Give the position of every leukocyte visible.
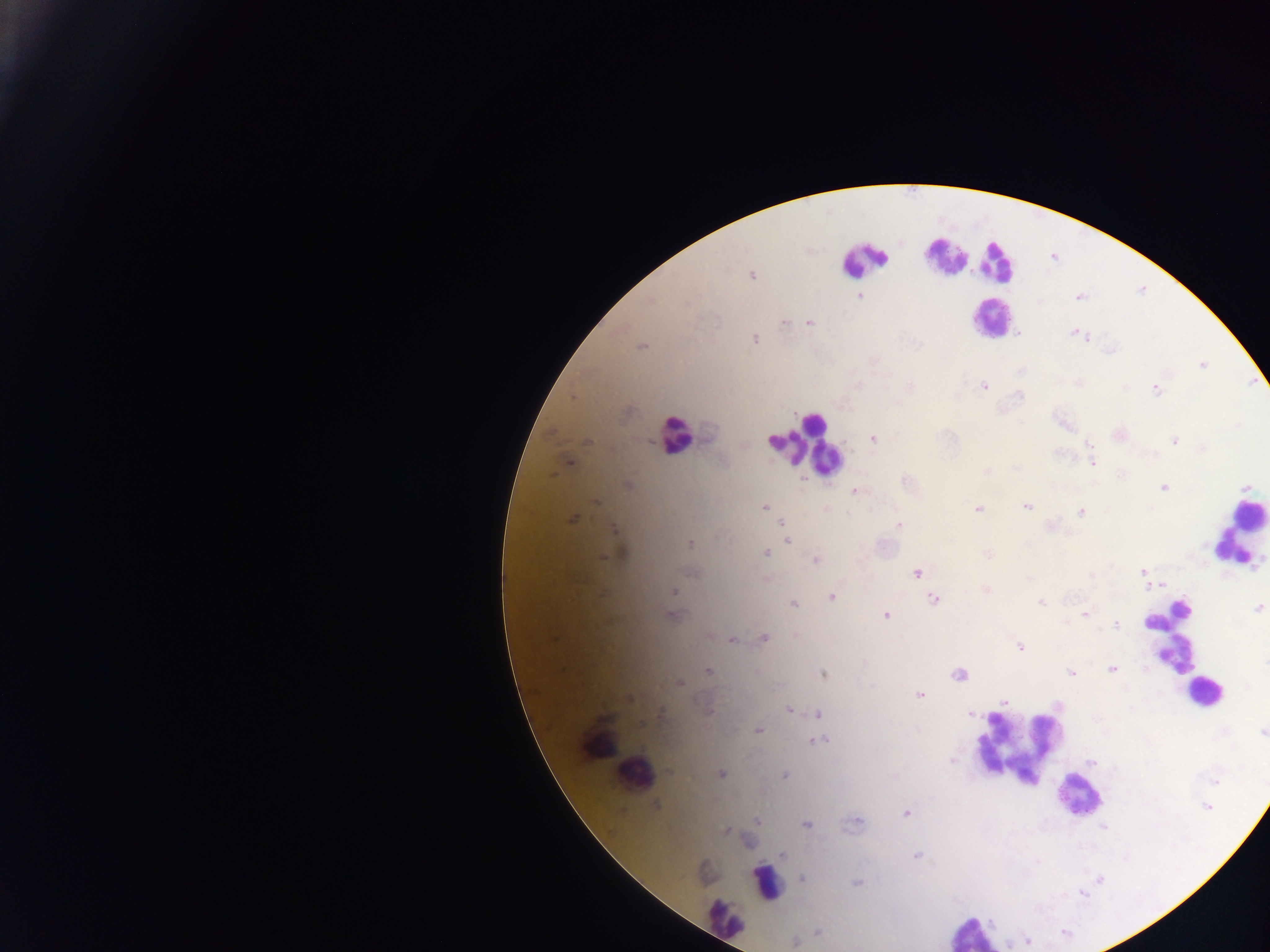
Approximate centers as {x, y} in pixels.
Leukocytes: {942, 255}, {862, 260}, {994, 262}, {989, 318}, {675, 435}, {803, 444}, {1239, 531}, {1172, 638}, {1202, 692}, {1016, 749}, {633, 772}, {1077, 797}, {765, 882}, {724, 919}, {971, 932}.

Malaria parasite locations: {752, 276}, {859, 295}, {1078, 298}, {784, 322}, {809, 323}, {1075, 333}, {1019, 334}, {1080, 336}, {755, 339}, {641, 347}, {1202, 365}, {984, 386}, {1156, 389}, {572, 398}, {1119, 435}, {873, 439}, {1175, 440}, {1090, 444}, {569, 462}, {1092, 462}, {986, 471}, {627, 484}, {1246, 487}, {1163, 488}, {855, 491}, {595, 501}, {1027, 506}, {764, 507}, {978, 509}, {1081, 512}, {571, 520}, {782, 524}, {898, 524}, {1052, 526}, {613, 529}, {788, 540}, {690, 544}, {766, 553}, {987, 554}, {816, 560}, {1143, 572}, {917, 573}, {692, 574}, {766, 578}, {1028, 578}, {1162, 585}, {1149, 586}, {986, 590}, {674, 591}, {831, 596}, {934, 599}, {1040, 603}, {794, 604}, {1258, 608}, {1085, 614}, {886, 615}, {673, 616}, {1115, 626}, {796, 636}, {764, 638}, {733, 640}, {1020, 646}, {1265, 662}, {1113, 669}, {709, 672}, {958, 673}, {1071, 673}, {823, 675}, {680, 683}, {919, 695}, {629, 698}, {1004, 701}, {789, 710}, {818, 714}, {971, 714}, {758, 730}, {1263, 732}, {819, 741}, {951, 760}, {1092, 762}, {721, 774}, {784, 776}, {656, 804}, {1206, 807}, {907, 813}, {756, 820}, {857, 822}, {806, 825}, {725, 831}, {783, 855}, {917, 856}, {802, 878}, {857, 883}, {817, 932}, {795, 941}. Photographed through a microscope with a mobile-phone camera. One field of view. Sample from Ghana. Thick blood smear. Image is 1270×952 pixels.